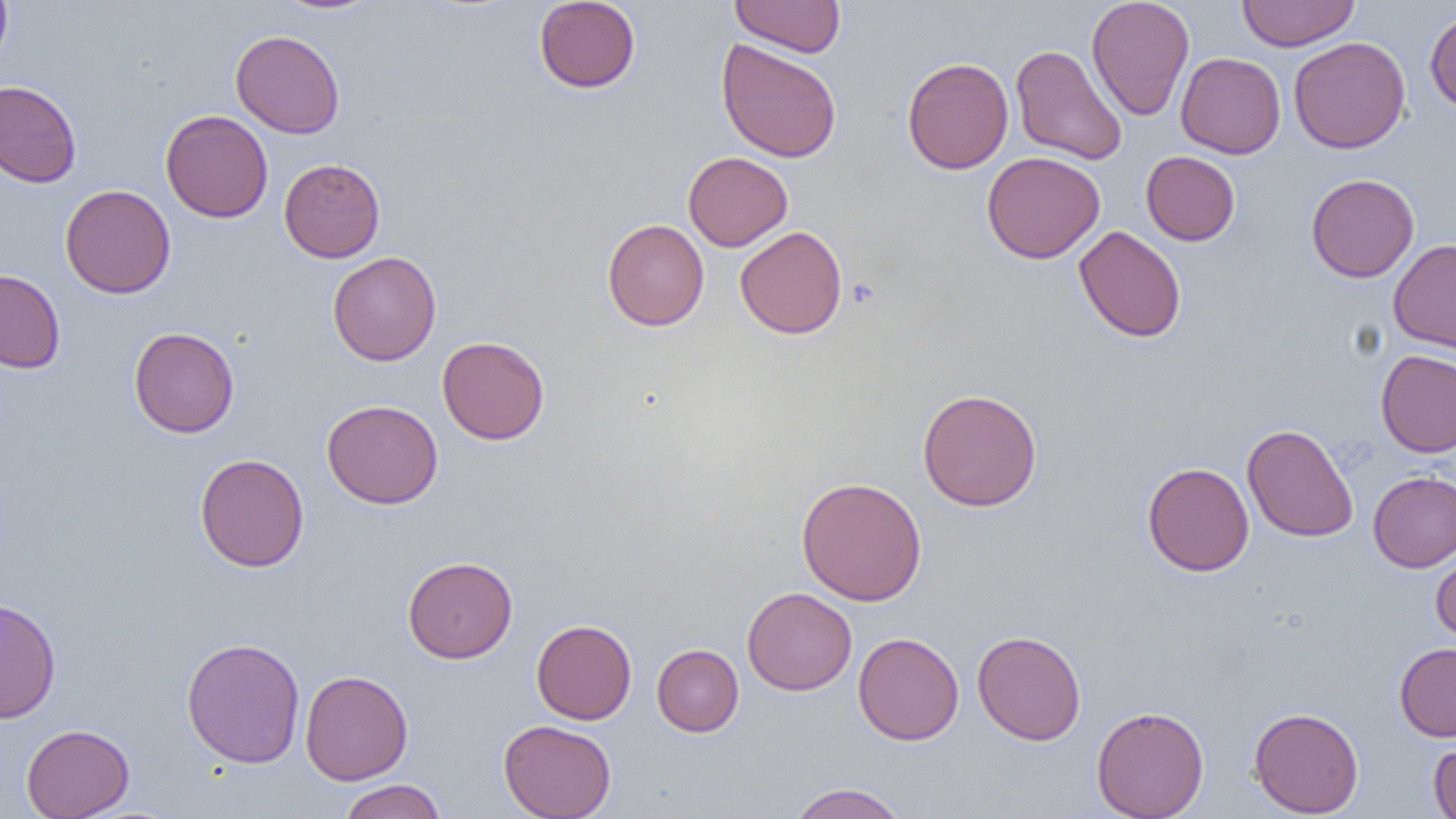
Approximate bounding boxes as (x1, y1, x2, y2) in pixels. Uninfected red blood cell locations: (0, 0, 13, 69), (274, 0, 383, 15), (534, 0, 641, 93), (730, 0, 846, 57), (1086, 0, 1195, 121), (1236, 0, 1361, 51), (1424, 8, 1456, 117), (230, 30, 345, 138), (1288, 36, 1410, 154), (716, 39, 842, 163), (1010, 45, 1127, 165), (1175, 52, 1286, 158), (902, 57, 1014, 174), (0, 80, 82, 188), (161, 109, 273, 223), (683, 151, 793, 251), (1141, 151, 1240, 245), (982, 152, 1105, 263), (279, 158, 385, 263), (1306, 173, 1419, 282), (60, 184, 176, 299), (602, 219, 709, 331), (735, 226, 847, 339), (1073, 226, 1186, 343), (1388, 238, 1456, 355), (327, 251, 441, 365), (0, 269, 65, 373), (129, 327, 240, 438), (437, 336, 549, 445), (1376, 349, 1456, 458), (917, 388, 1042, 511), (322, 399, 443, 509), (1242, 424, 1358, 542), (194, 453, 309, 572), (1142, 461, 1254, 577), (1368, 471, 1456, 572), (796, 476, 927, 606), (1430, 545, 1456, 642), (403, 556, 518, 663), (742, 588, 857, 696), (0, 596, 62, 724), (531, 619, 637, 724), (972, 630, 1087, 745), (853, 632, 965, 745), (181, 637, 306, 768), (1395, 642, 1456, 741), (652, 644, 743, 737), (300, 669, 413, 785), (1091, 705, 1209, 818), (1248, 707, 1364, 817), (499, 719, 616, 819), (21, 724, 135, 819), (1428, 734, 1456, 819), (338, 779, 447, 819), (785, 782, 910, 819). Platelet locations: (846, 278, 879, 309). Slide-level diagnosis: negative for blood parasites. One field of a larger specimen. Thin blood film. 1000x magnification. Image is 1456×819 pixels. Light microscopy.